State the blood parasite species.
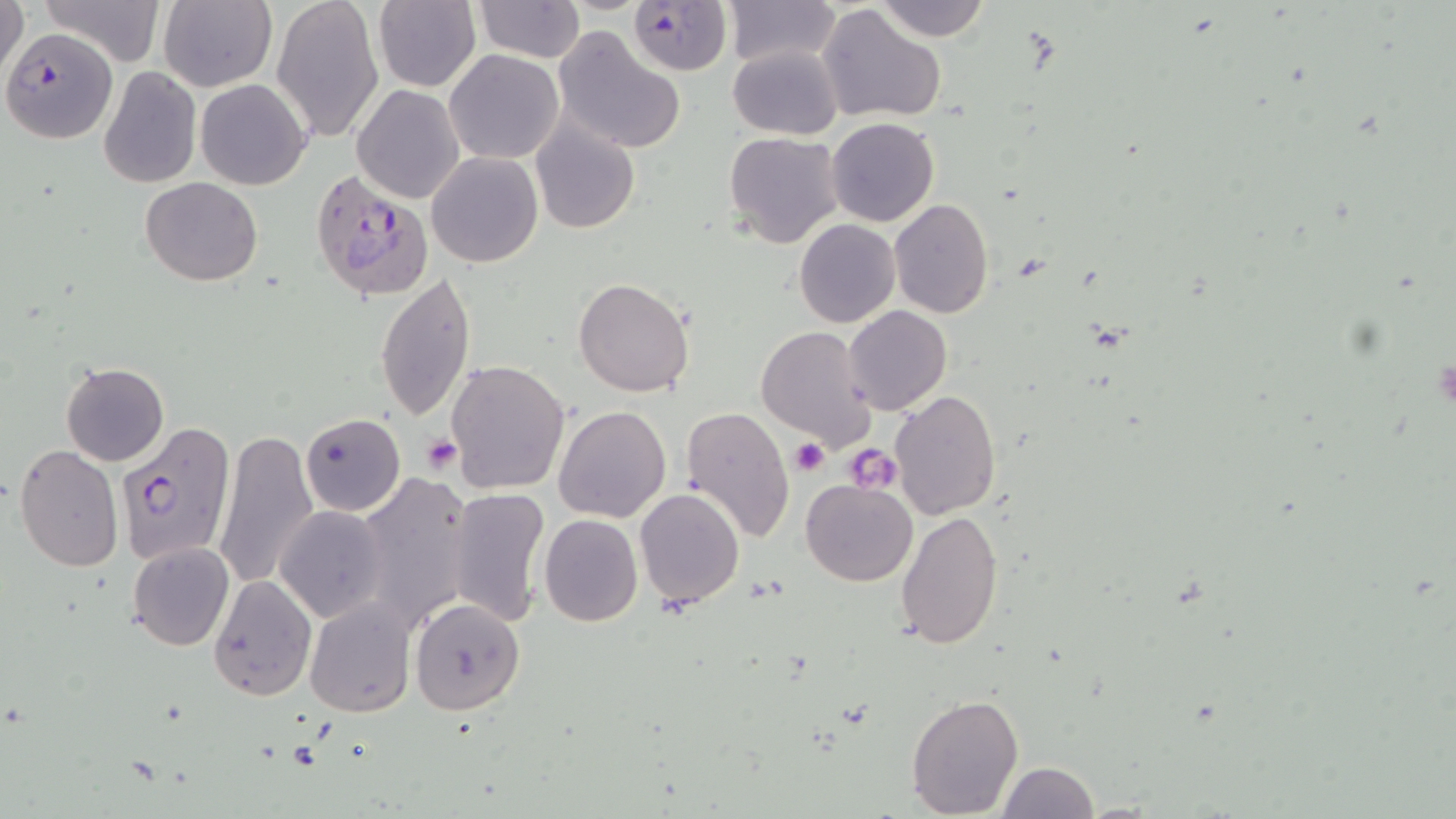

Plasmodium falciparum.

image size = 1456×819 pixels
uninfected red blood cell locations = approximate bounding boxes as named x1/y1/x2/y2 corners in pixels: (x1=0, y1=0, x2=28, y2=83), (x1=35, y1=0, x2=165, y2=69), (x1=157, y1=0, x2=276, y2=92), (x1=271, y1=0, x2=384, y2=144), (x1=373, y1=0, x2=482, y2=92), (x1=474, y1=0, x2=583, y2=62), (x1=723, y1=0, x2=840, y2=69), (x1=874, y1=0, x2=991, y2=42), (x1=818, y1=4, x2=947, y2=122), (x1=552, y1=26, x2=688, y2=154), (x1=728, y1=45, x2=843, y2=140), (x1=445, y1=49, x2=563, y2=164), (x1=98, y1=67, x2=201, y2=188), (x1=195, y1=78, x2=312, y2=189), (x1=352, y1=83, x2=465, y2=203), (x1=825, y1=117, x2=939, y2=227), (x1=531, y1=118, x2=640, y2=235), (x1=722, y1=132, x2=844, y2=247), (x1=425, y1=151, x2=543, y2=267), (x1=140, y1=176, x2=261, y2=286), (x1=889, y1=198, x2=994, y2=319), (x1=795, y1=219, x2=900, y2=327), (x1=375, y1=272, x2=477, y2=420), (x1=573, y1=277, x2=695, y2=398), (x1=844, y1=306, x2=952, y2=415), (x1=755, y1=326, x2=876, y2=449), (x1=445, y1=358, x2=571, y2=495), (x1=61, y1=361, x2=170, y2=466), (x1=889, y1=389, x2=1000, y2=519), (x1=553, y1=405, x2=671, y2=523), (x1=680, y1=406, x2=795, y2=543), (x1=300, y1=413, x2=405, y2=516), (x1=212, y1=430, x2=318, y2=589), (x1=13, y1=444, x2=123, y2=572), (x1=354, y1=474, x2=472, y2=629), (x1=800, y1=478, x2=920, y2=587), (x1=447, y1=487, x2=552, y2=628), (x1=634, y1=488, x2=744, y2=607), (x1=275, y1=506, x2=391, y2=624), (x1=895, y1=508, x2=1005, y2=652), (x1=539, y1=513, x2=642, y2=627), (x1=285, y1=532, x2=402, y2=699), (x1=127, y1=542, x2=234, y2=651), (x1=208, y1=575, x2=316, y2=700), (x1=304, y1=597, x2=416, y2=718), (x1=410, y1=598, x2=525, y2=713), (x1=905, y1=694, x2=1025, y2=818), (x1=996, y1=761, x2=1100, y2=818)
magnification = 1000x
Plasmodium falciparum-infected red blood cell locations = approximate bounding boxes as named x1/y1/x2/y2 corners in pixels: (x1=628, y1=1, x2=732, y2=76), (x1=2, y1=26, x2=118, y2=144), (x1=309, y1=170, x2=436, y2=302), (x1=116, y1=422, x2=234, y2=563)
modality = light microscopy
preparation = thin blood film
field of view = one of a larger specimen
platelet locations = approximate bounding boxes as named x1/y1/x2/y2 corners in pixels: (x1=422, y1=436, x2=463, y2=475), (x1=791, y1=440, x2=828, y2=476), (x1=844, y1=444, x2=900, y2=490)
stain = May-Grünwald-Giemsa